Assess this cell for malaria.
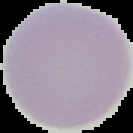
Uninfected.

Segmented cell region on a black background. From a thin blood smear. Image is 133×133 pixels.